Classify the preparation.
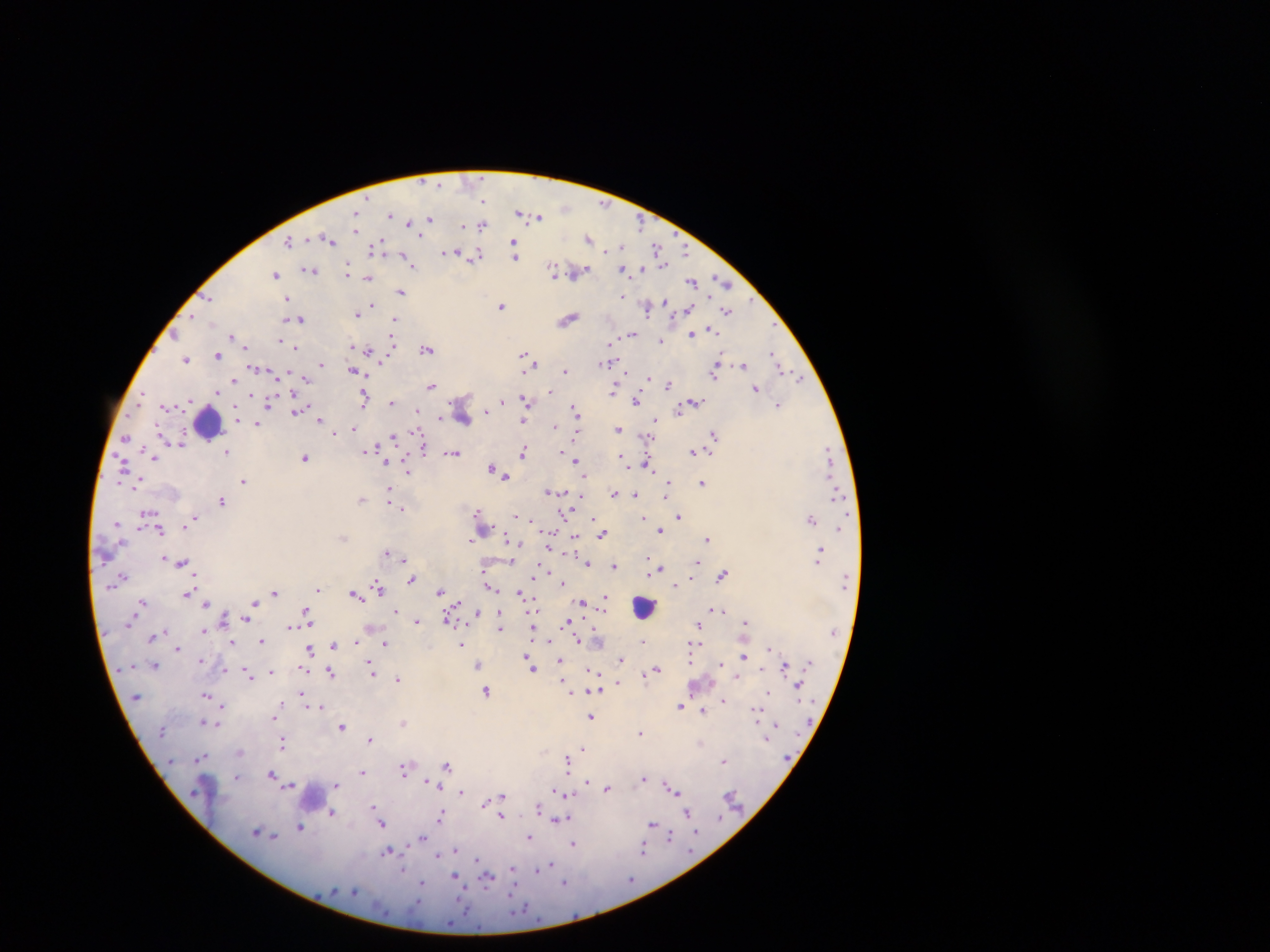

This is a thick smear.

Approximate centers as {x, y} in pixels. Plasmodium parasite locations: {483, 200}, {519, 212}, {356, 214}, {391, 215}, {538, 217}, {429, 218}, {408, 223}, {640, 224}, {463, 226}, {482, 226}, {329, 238}, {589, 238}, {289, 240}, {514, 242}, {621, 246}, {656, 247}, {373, 248}, {608, 249}, {686, 251}, {446, 253}, {515, 255}, {476, 256}, {403, 257}, {410, 264}, {663, 265}, {626, 269}, {641, 269}, {309, 270}, {348, 270}, {553, 270}, {562, 272}, {579, 272}, {276, 274}, {368, 278}, {692, 281}, {722, 281}, {401, 292}, {622, 296}, {287, 297}, {209, 299}, {369, 305}, {502, 306}, {648, 308}, {688, 309}, {727, 311}, {357, 314}, {193, 315}, {301, 319}, {568, 319}, {395, 320}, {711, 330}, {176, 334}, {692, 334}, {232, 335}, {632, 335}, {281, 340}, {393, 341}, {661, 341}, {611, 343}, {246, 346}, {353, 346}, {296, 347}, {426, 349}, {368, 352}, {773, 353}, {217, 356}, {524, 356}, {186, 359}, {718, 360}, {532, 361}, {608, 361}, {321, 364}, {743, 365}, {779, 368}, {354, 371}, {565, 371}, {714, 373}, {649, 377}, {305, 379}, {800, 379}, {234, 380}, {431, 385}, {669, 385}, {756, 389}, {614, 390}, {550, 391}, {218, 392}, {141, 395}, {253, 396}, {525, 398}, {364, 400}, {269, 401}, {503, 401}, {636, 401}, {696, 401}, {391, 402}, {778, 405}, {683, 407}, {573, 408}, {416, 411}, {486, 411}, {679, 411}, {296, 412}, {441, 417}, {320, 419}, {655, 419}, {523, 421}, {257, 425}, {554, 426}, {354, 429}, {333, 430}, {617, 430}, {576, 434}, {714, 435}, {126, 437}, {394, 437}, {647, 438}, {181, 441}, {423, 449}, {367, 450}, {226, 451}, {561, 451}, {523, 452}, {692, 452}, {828, 452}, {453, 453}, {621, 456}, {153, 457}, {305, 457}, {577, 460}, {386, 462}, {625, 462}, {648, 466}, {124, 468}, {491, 468}, {407, 471}, {503, 475}, {243, 481}, {702, 483}, {668, 484}, {389, 490}, {550, 492}, {614, 493}, {636, 494}, {836, 494}, {582, 496}, {666, 496}, {362, 499}, {222, 501}, {398, 507}, {402, 509}, {477, 511}, {568, 513}, {518, 516}, {678, 517}, {592, 518}, {644, 518}, {192, 519}, {811, 519}, {533, 520}, {839, 528}, {160, 530}, {660, 530}, {602, 535}, {344, 537}, {575, 538}, {507, 539}, {708, 539}, {470, 541}, {519, 544}, {550, 547}, {820, 552}, {386, 553}, {164, 558}, {403, 559}, {182, 562}, {698, 562}, {405, 563}, {588, 563}, {614, 566}, {661, 568}, {648, 572}, {535, 575}, {723, 575}, {123, 577}, {412, 579}, {563, 583}, {676, 585}, {490, 586}, {378, 588}, {318, 589}, {440, 591}, {276, 592}, {519, 593}, {187, 594}, {354, 595}, {604, 597}, {142, 601}, {254, 603}, {583, 603}, {205, 604}, {712, 608}, {721, 610}, {396, 611}, {307, 617}, {449, 617}, {500, 617}, {246, 619}, {417, 621}, {745, 621}, {566, 622}, {698, 625}, {500, 628}, {204, 631}, {153, 637}, {550, 640}, {262, 641}, {578, 641}, {643, 641}, {356, 642}, {232, 643}, {385, 643}, {337, 644}, {462, 645}, {178, 648}, {310, 648}, {769, 648}, {744, 656}, {620, 659}, {528, 660}, {560, 661}, {691, 661}, {721, 663}, {155, 665}, {478, 665}, {785, 666}, {532, 667}, {762, 668}, {657, 669}, {373, 671}, {591, 671}, {271, 672}, {331, 673}, {249, 675}, {736, 676}, {398, 679}, {617, 684}, {798, 684}, {486, 691}, {570, 692}, {768, 692}, {597, 693}, {301, 694}, {206, 695}, {723, 700}, {222, 705}, {321, 706}, {680, 706}, {703, 711}, {756, 714}, {274, 717}, {591, 717}, {203, 722}, {404, 723}, {216, 724}, {776, 724}, {342, 727}, {641, 732}, {371, 740}, {702, 742}, {284, 743}, {583, 748}, {239, 752}, {202, 757}, {568, 757}, {724, 761}, {566, 762}, {446, 766}, {404, 770}, {362, 772}, {271, 773}, {236, 777}, {644, 779}, {426, 781}, {588, 782}, {290, 785}, {336, 785}, {608, 788}, {556, 790}, {674, 790}, {461, 792}, {561, 793}, {503, 798}, {486, 803}, {374, 807}, {538, 808}, {377, 811}, {332, 812}, {687, 813}, {441, 815}, {502, 816}, {560, 819}, {567, 819}, {381, 822}, {652, 823}, {301, 827}, {257, 831}, {697, 832}, {274, 837}, {422, 837}, {531, 837}, {670, 837}, {573, 844}, {644, 848}, {455, 850}, {387, 851}, {437, 856}, {477, 860}, {551, 864}, {544, 867}, {403, 869}, {537, 870}, {513, 872}, {487, 877}, {456, 878}, {564, 882}, {422, 883}. Leukocyte locations: {208, 423}, {644, 606}, {313, 792}. Image is 1270×952 pixels. One field of view. Photographed through a microscope with a mobile-phone camera. Sample from Ghana.